Point out each Plasmodium parasite.
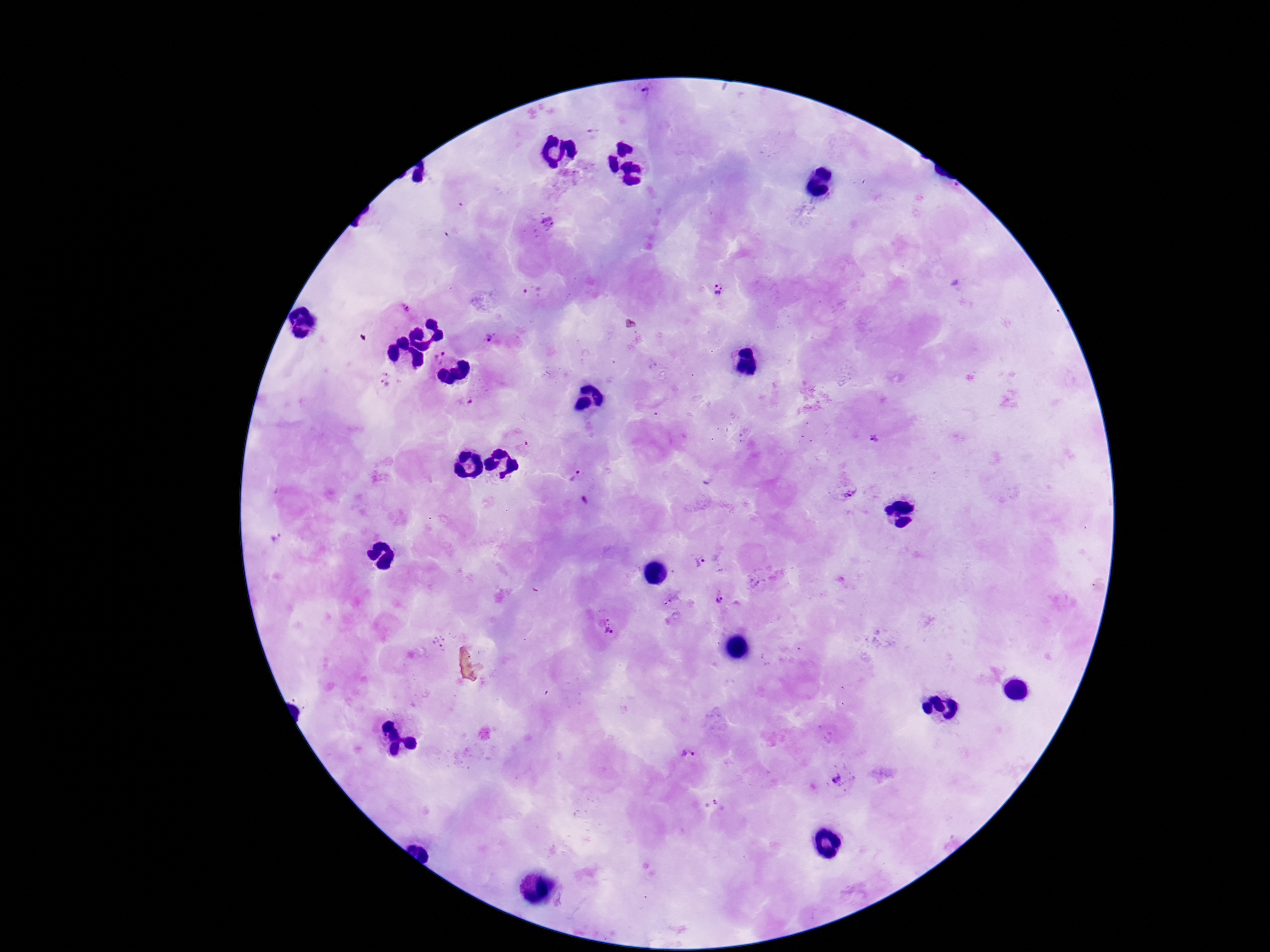

Approximate centers as (x, y) in pixels.
Plasmodium parasites: (646, 96), (549, 224), (718, 290), (533, 292), (407, 306), (492, 338), (440, 355), (384, 380), (465, 402), (874, 439), (577, 475), (849, 493), (276, 540), (700, 560), (718, 597), (671, 600), (609, 628), (689, 757), (836, 779).

field of view = single
capture = smartphone camera through the microscope eyepiece
image size = 1270×952 pixels
magnification = 100x
preparation = thick peripheral-blood smear
stain = Giemsa
patient malaria status = infected